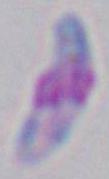
Summary:
  - Modality: photomicrograph
  - Magnification: 1000x
  - Identification: Toxoplasma gondii